Classify this cell by malaria status.
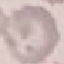

Uninfected.

Acquired by smartphone through the microscope eyepiece. Giemsa stain. Thin blood film. Cell patch, automatically extracted from a larger field of view and resized to 64 × 64 pixels.